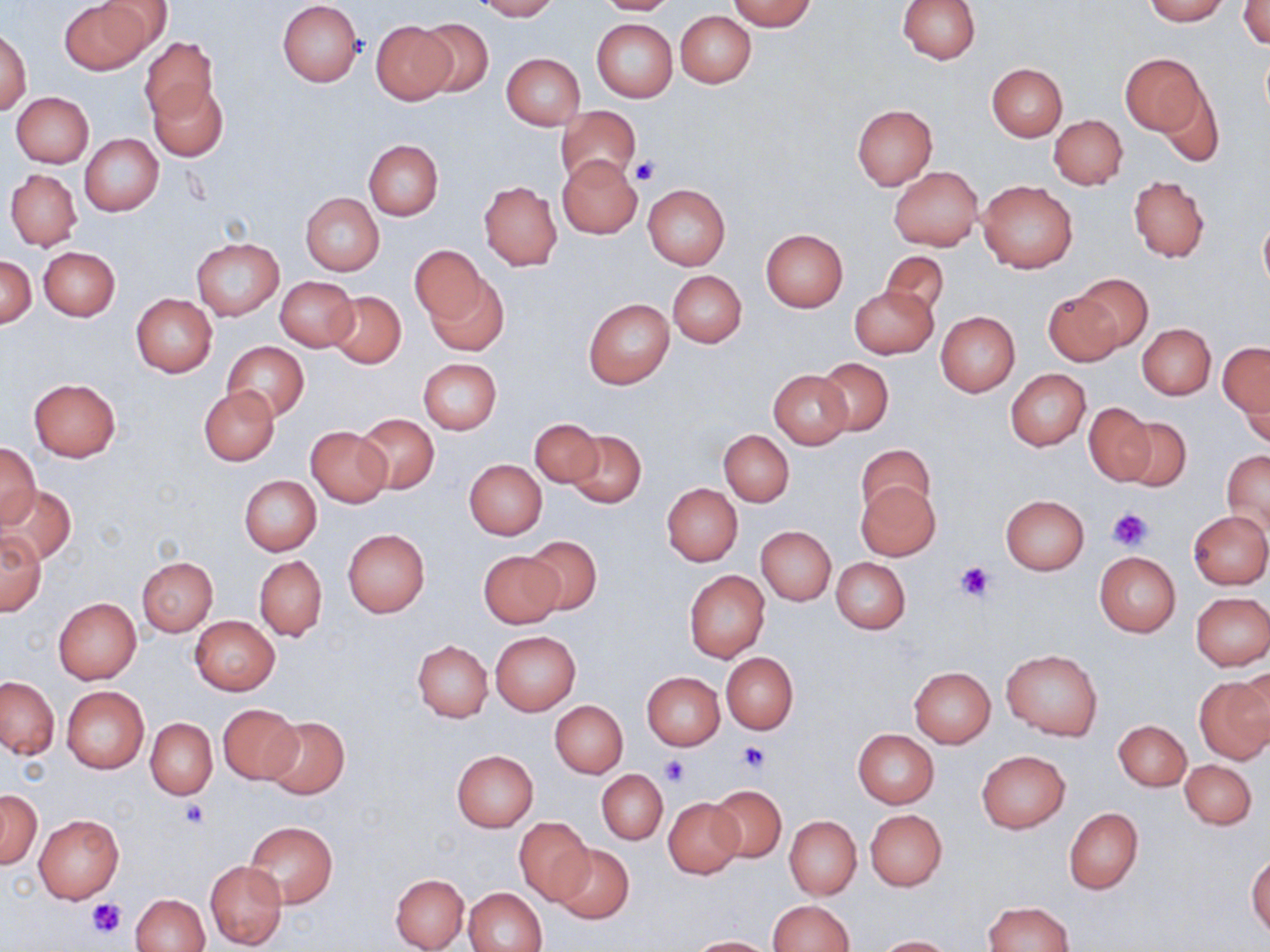

Approximate bounding boxes as (x1,y1)-(x2,y2) corner pairs in pixels. Uninfected red blood cell locations: (60,0)-(150,74), (475,0)-(558,20), (594,0)-(680,15), (727,0)-(816,31), (898,0)-(981,64), (1143,0)-(1227,24), (91,1)-(175,55), (276,1)-(364,86), (1239,1)-(1269,49), (676,11)-(755,88), (415,16)-(494,99), (591,18)-(678,103), (371,21)-(455,103), (1,28)-(32,116), (139,36)-(217,121), (1259,41)-(1270,125), (1120,53)-(1208,136), (502,54)-(584,130), (987,62)-(1067,141), (1153,79)-(1222,165), (149,83)-(227,161), (11,91)-(93,166), (556,105)-(641,185), (852,105)-(936,189), (1050,115)-(1127,189), (81,134)-(163,215), (363,139)-(443,221), (557,154)-(643,240), (888,166)-(982,250), (6,168)-(82,251), (1129,176)-(1210,262), (978,178)-(1078,273), (479,180)-(563,270), (643,183)-(730,271), (301,193)-(384,275), (1258,211)-(1270,298), (761,229)-(848,313), (192,237)-(284,320), (39,246)-(120,320), (410,246)-(485,326), (880,251)-(951,320), (1,256)-(36,327), (668,270)-(746,348), (426,272)-(509,357), (1069,273)-(1154,353), (275,276)-(360,352), (849,285)-(938,359), (326,290)-(406,368), (1043,292)-(1123,366), (131,293)-(217,377), (584,299)-(675,390), (936,312)-(1020,395), (1137,323)-(1215,399), (222,342)-(309,420), (1219,343)-(1270,418), (418,358)-(502,434), (816,358)-(893,436), (1006,369)-(1090,450), (769,370)-(852,449), (1235,375)-(1270,450), (29,378)-(121,460), (200,386)-(280,464), (1084,403)-(1155,485), (356,415)-(439,492), (1119,415)-(1192,492), (530,418)-(603,487), (306,427)-(392,508), (566,430)-(645,510), (719,430)-(794,507), (1,442)-(39,528), (856,442)-(935,518), (1223,451)-(1269,536), (464,459)-(547,540), (239,475)-(321,555), (855,481)-(940,561), (663,484)-(742,566), (3,486)-(75,562), (999,495)-(1089,575), (1189,511)-(1270,588), (756,526)-(836,605), (343,529)-(430,617), (0,530)-(46,615), (522,535)-(601,614), (479,551)-(566,627), (1095,552)-(1181,637), (138,557)-(217,636), (255,557)-(327,641), (830,557)-(910,635), (685,570)-(770,662), (1190,592)-(1268,670), (53,597)-(141,684), (190,616)-(280,695), (490,631)-(581,715), (413,640)-(492,723), (1002,650)-(1103,740), (722,653)-(797,733), (909,667)-(995,748), (1239,667)-(1270,749), (642,672)-(725,750), (1195,673)-(1270,765), (0,677)-(58,759), (61,686)-(149,772), (550,700)-(628,777), (218,703)-(302,785), (262,715)-(350,799), (145,718)-(217,798), (1114,721)-(1190,790), (853,729)-(939,807), (452,750)-(538,832), (977,750)-(1069,832), (1180,759)-(1256,829), (597,771)-(667,843), (706,785)-(786,862), (0,790)-(41,868), (664,798)-(744,878), (1064,807)-(1143,894), (865,809)-(947,891), (34,814)-(124,902), (784,816)-(861,900), (514,817)-(595,904), (245,821)-(338,906), (553,843)-(634,923), (1247,854)-(1270,937), (204,860)-(287,951), (390,873)-(470,951), (134,884)-(284,952), (463,887)-(547,952), (131,893)-(210,952), (766,900)-(854,952), (983,900)-(1073,952), (876,935)-(954,952), (685,937)-(777,952). Platelet locations: (632,157)-(660,184), (1108,507)-(1154,551), (956,561)-(996,603), (739,742)-(768,773), (660,757)-(690,787), (178,799)-(210,827), (87,898)-(126,937). Slide-level diagnosis: negative for blood parasites. May-Grünwald-Giemsa-stained preparation. 1000x magnification. Thin blood smear. One field of a larger specimen. Image is 1270×952 pixels. Optical microscopy.